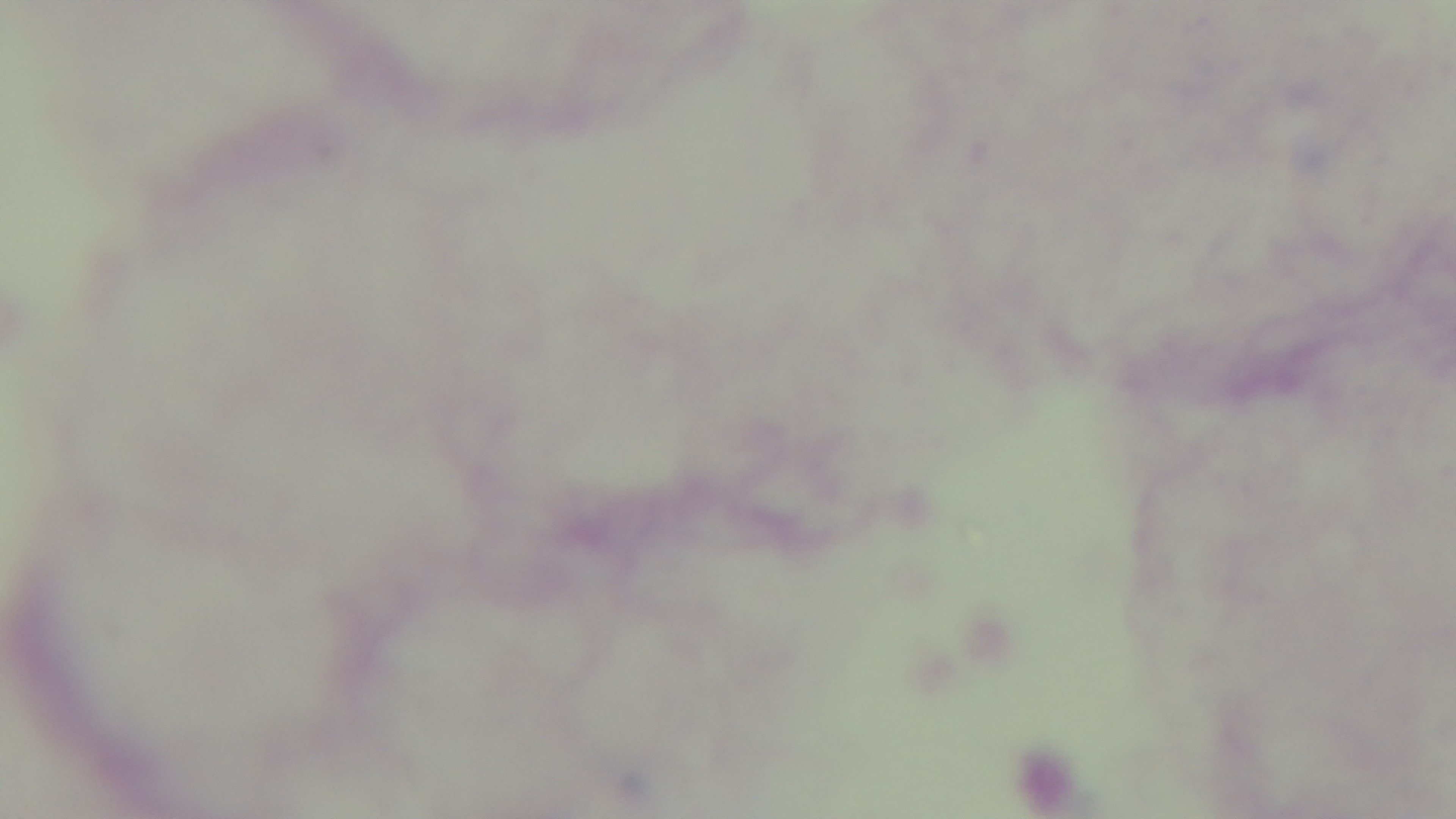

Photomicrograph. Malaria status: uninfected. 100x oil-immersion objective. Giemsa stain. Preparation: thick smear. One field from the slide. Captured with a mounted 4K digital camera.